State which cell type is depicted.
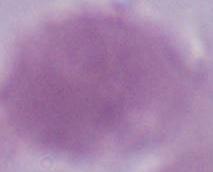
An erythrocyte.

Photomicrograph. Captured at 1000x magnification.